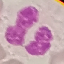

Summary:
  - Malaria status: uninfected
  - Image type: automatically extracted cell patch, resized to 64 × 64 pixels
  - Stain: Giemsa
  - Capture: smartphone camera at the microscope eyepiece
  - Preparation: thin blood smear